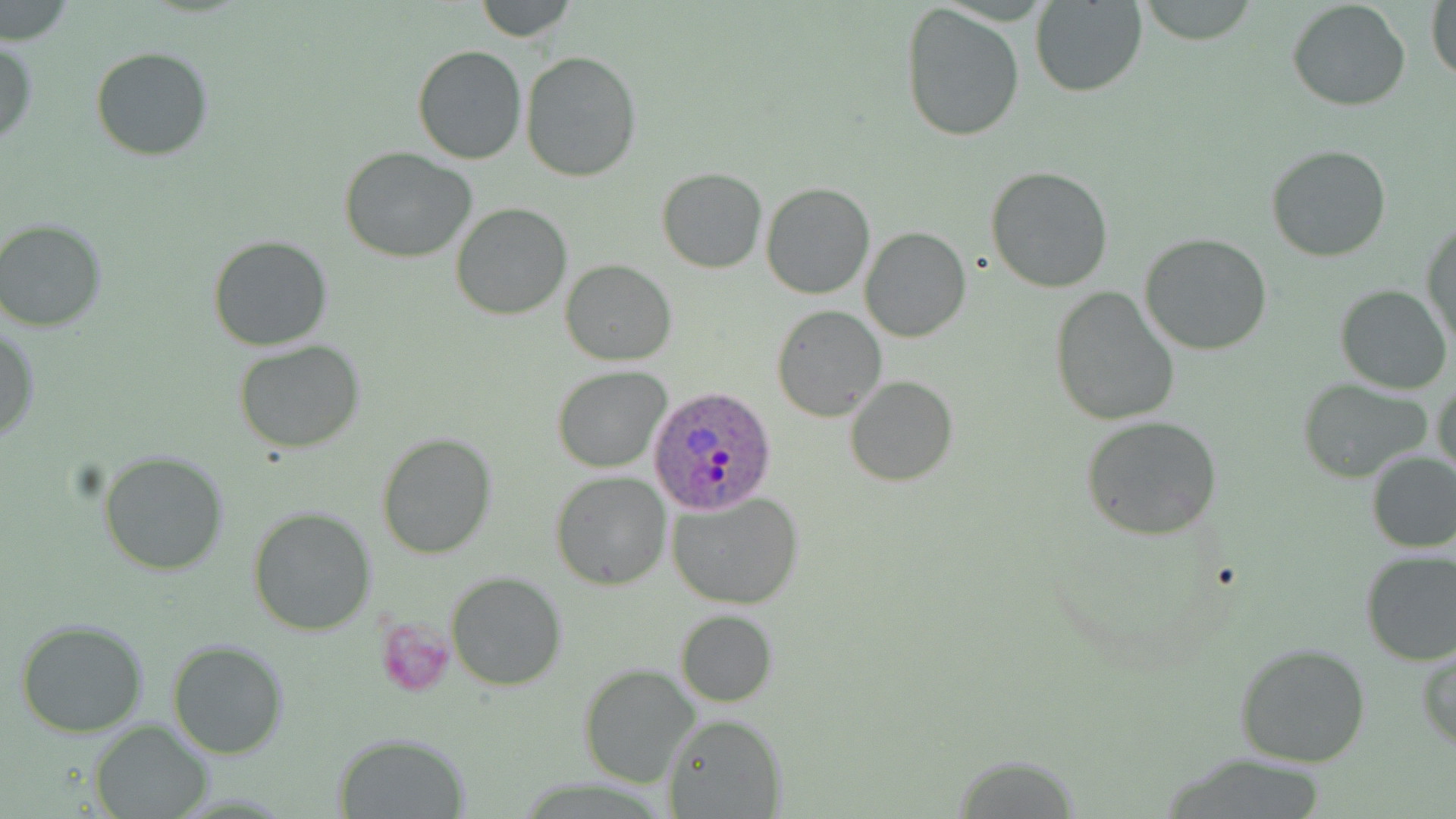
Summary:
  - Coordinate format: approximate bounding boxes as [x1, y1, x2, y2] in pixels
  - Plasmodium ovale-infected red blood cell locations: [646, 388, 777, 512]
  - Platelet locations: [377, 619, 455, 696]
  - Uninfected red blood cell locations: [474, 0, 577, 42], [1135, 0, 1258, 43], [1427, 0, 1456, 87], [1029, 1, 1146, 97], [1287, 1, 1411, 112], [900, 4, 1026, 143], [0, 37, 38, 147], [412, 45, 526, 165], [91, 47, 214, 161], [520, 51, 643, 181], [1265, 143, 1394, 263], [339, 148, 477, 262], [984, 166, 1114, 293], [656, 168, 768, 274], [760, 182, 876, 300], [451, 201, 572, 320], [0, 218, 109, 333], [1422, 218, 1455, 353], [860, 227, 970, 342], [1139, 233, 1273, 356], [209, 235, 332, 352], [560, 259, 675, 365], [1335, 285, 1453, 394], [1049, 287, 1181, 427], [772, 305, 886, 422], [1, 326, 38, 443], [233, 340, 367, 454], [552, 365, 671, 473], [1433, 374, 1456, 483], [846, 376, 957, 487], [1298, 379, 1432, 483], [1081, 416, 1224, 539], [376, 432, 497, 559], [98, 449, 231, 577], [1364, 451, 1456, 553], [551, 471, 671, 589], [668, 492, 805, 607], [247, 507, 376, 636], [1359, 549, 1456, 666], [445, 572, 567, 692], [674, 610, 776, 707], [15, 619, 151, 736], [168, 638, 289, 758], [1232, 641, 1372, 769], [1418, 646, 1456, 750], [580, 663, 701, 789], [664, 714, 784, 818], [88, 719, 213, 818], [335, 733, 469, 817], [946, 751, 1083, 815]
  - Slide-level diagnosis: Plasmodium ovale
  - Magnification: 1000x
  - Stain: May-Grünwald-Giemsa
  - Modality: light microscopy
  - Field of view: one of a larger specimen
  - Preparation: thin blood film
  - Image size: 1456×819 pixels